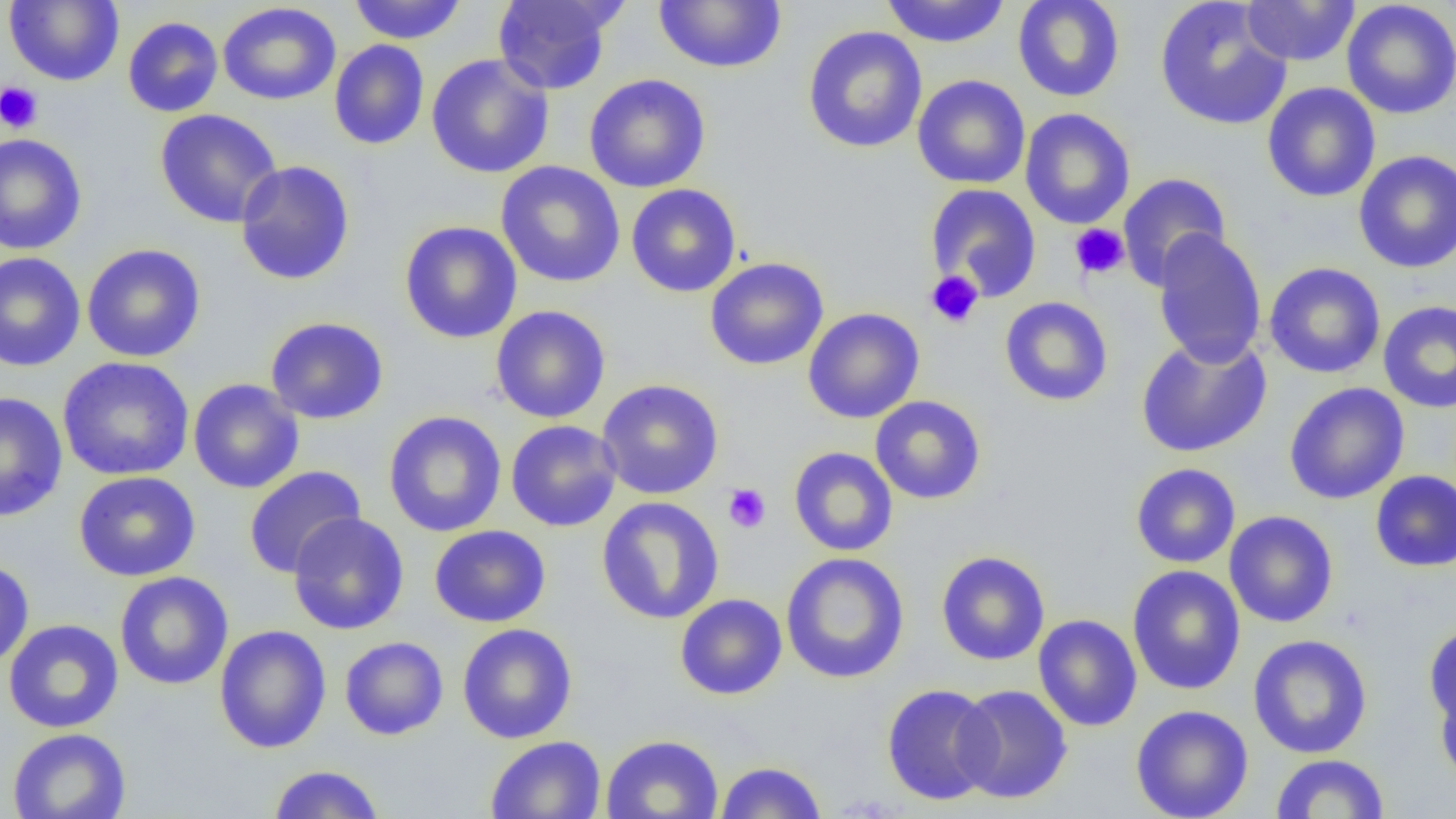

Summary:
  - Coordinate format: approximate bounding boxes as (x1, y1, x2, y2) in pixels
  - Platelet locations: (0, 81, 43, 134), (1070, 224, 1130, 279), (925, 270, 984, 329), (723, 484, 771, 533)
  - Uninfected red blood cell locations: (4, 0, 124, 86), (348, 0, 468, 44), (492, 0, 621, 95), (880, 0, 1011, 48), (1012, 0, 1126, 102), (1154, 0, 1292, 131), (1342, 0, 1456, 120), (653, 1, 787, 73), (1240, 1, 1360, 66), (217, 2, 342, 105), (123, 16, 224, 117), (802, 26, 928, 153), (329, 40, 430, 151), (426, 53, 554, 179), (584, 73, 711, 193), (912, 74, 1030, 190), (1262, 82, 1381, 203), (154, 108, 282, 228), (1020, 108, 1135, 229), (0, 133, 87, 255), (1353, 149, 1456, 273), (235, 160, 355, 286), (496, 161, 625, 288), (1117, 172, 1232, 291), (626, 183, 742, 298), (925, 183, 1042, 301), (399, 220, 523, 344), (1151, 229, 1267, 368), (81, 243, 206, 363), (0, 251, 86, 372), (704, 257, 829, 371), (1263, 262, 1386, 379), (999, 296, 1113, 407), (1378, 300, 1456, 414), (490, 305, 611, 423), (803, 307, 925, 424), (265, 316, 389, 424), (1135, 334, 1273, 458), (56, 356, 194, 481), (188, 378, 305, 494), (597, 379, 724, 500), (1283, 382, 1410, 504), (0, 391, 68, 522), (869, 395, 986, 505), (383, 411, 507, 537), (506, 419, 622, 532), (788, 446, 898, 557), (1130, 463, 1241, 568), (243, 465, 366, 579), (1370, 470, 1456, 573), (73, 471, 201, 582), (596, 496, 725, 624), (1224, 510, 1338, 628), (287, 512, 410, 635), (429, 525, 551, 628), (936, 551, 1050, 665), (780, 552, 910, 684), (0, 558, 35, 669), (1127, 565, 1245, 695), (114, 571, 234, 690), (675, 593, 788, 700), (1033, 614, 1142, 732), (3, 619, 124, 734), (457, 623, 577, 744), (1423, 623, 1455, 732), (213, 625, 332, 754), (1248, 634, 1373, 759), (339, 636, 449, 740), (1434, 675, 1456, 789), (881, 684, 999, 806), (953, 684, 1072, 805), (1130, 704, 1254, 819), (6, 728, 131, 819), (601, 733, 724, 819), (485, 735, 606, 818), (1269, 753, 1391, 818), (715, 761, 827, 818), (268, 765, 385, 818)
  - Slide-level diagnosis: negative for blood parasites
  - Magnification: 1000x
  - Modality: optical microscopy
  - Preparation: thin blood film
  - Image size: 1456×819 pixels
  - Field of view: single